State which parasite is depicted.
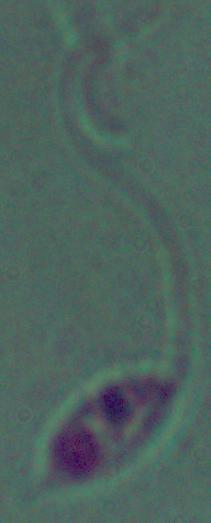
This is Leishmania.

Micrograph. Captured at 1000x magnification.